Locate and identify every blood parasite.
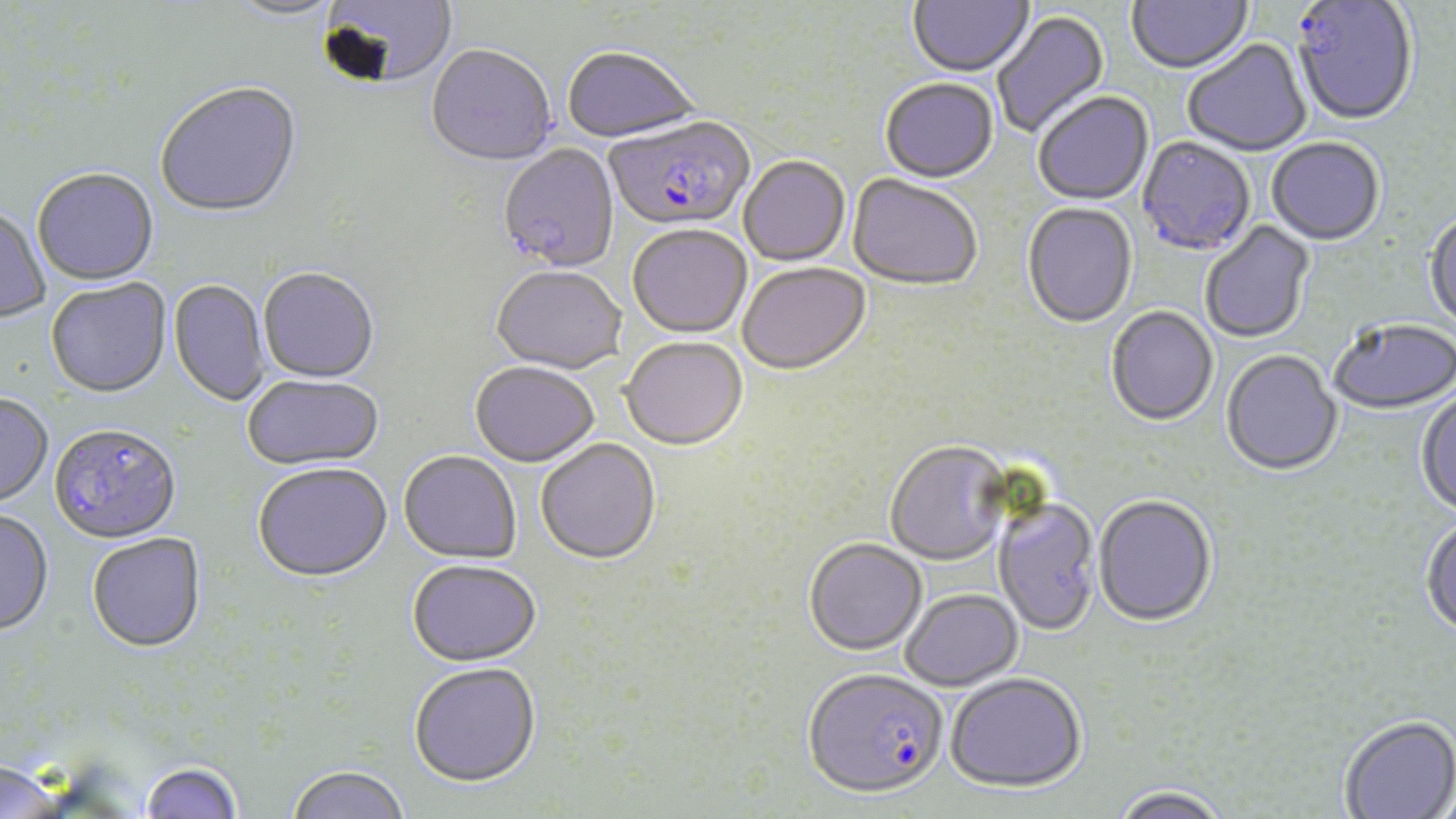

Approximate bounding boxes as [x1, y1, x2, y2] in pixels.
Plasmodium falciparum-infected red blood cells: [1291, 1, 1418, 129], [604, 118, 756, 235], [49, 426, 182, 547], [803, 671, 949, 803].
No Plasmodium ovale, Plasmodium malariae, Plasmodium vivax, Babesia divergens, or Trypanosoma brucei observed.

Uninfected red blood cell locations: [317, 0, 458, 91], [908, 0, 1034, 79], [1127, 0, 1253, 76], [223, 1, 345, 24], [993, 10, 1111, 139], [1183, 40, 1312, 158], [426, 47, 556, 169], [562, 49, 701, 147], [880, 80, 998, 185], [156, 84, 303, 221], [1034, 93, 1154, 206], [1136, 138, 1255, 258], [1267, 139, 1384, 247], [498, 145, 620, 274], [739, 158, 850, 268], [32, 170, 159, 287], [846, 175, 982, 293], [1022, 203, 1137, 330], [0, 208, 50, 324], [1424, 212, 1456, 336], [1200, 221, 1315, 344], [628, 226, 752, 340], [737, 265, 872, 378], [491, 269, 627, 376], [258, 270, 379, 385], [45, 280, 171, 400], [168, 280, 271, 408], [1106, 307, 1218, 428], [1329, 320, 1456, 416], [621, 339, 748, 453], [1221, 351, 1342, 478], [470, 364, 598, 469], [243, 377, 385, 472], [1415, 390, 1456, 517], [0, 395, 54, 510], [536, 440, 661, 567], [884, 443, 1012, 568], [399, 453, 521, 565], [253, 466, 392, 586], [1093, 497, 1217, 628], [993, 499, 1100, 638], [0, 511, 54, 638], [1420, 517, 1456, 640], [86, 534, 207, 655], [804, 540, 927, 658], [406, 563, 542, 670], [900, 590, 1023, 692], [408, 666, 542, 791], [945, 675, 1086, 796], [1339, 717, 1456, 819], [0, 762, 67, 819], [139, 762, 242, 819], [286, 767, 411, 819], [1110, 787, 1230, 819]. Slide-level diagnosis: Plasmodium falciparum. May-Grünwald-Giemsa stain. Light microscopy. Single field of view. Thin blood smear. Image is 1456×819 pixels. Captured at 1000x magnification.